Identify the cell.
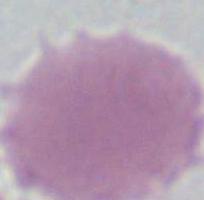

An erythrocyte.

Captured at 1000x magnification. Micrograph.